Describe the morphology of the red blood cells.
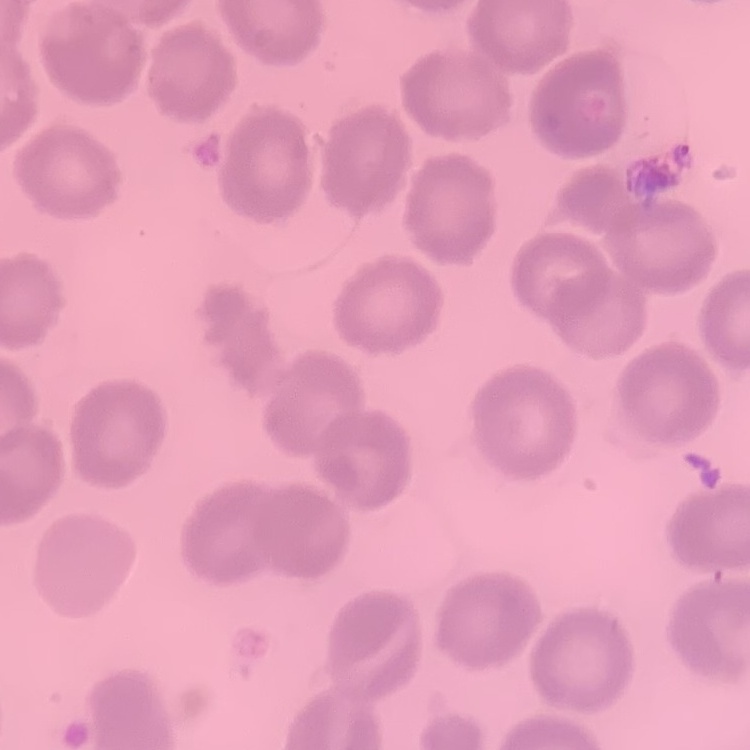

No rouleaux formation.

preparation = thin blood smear
image type = square crop of a larger photomicrograph
stain = Field's or Giemsa